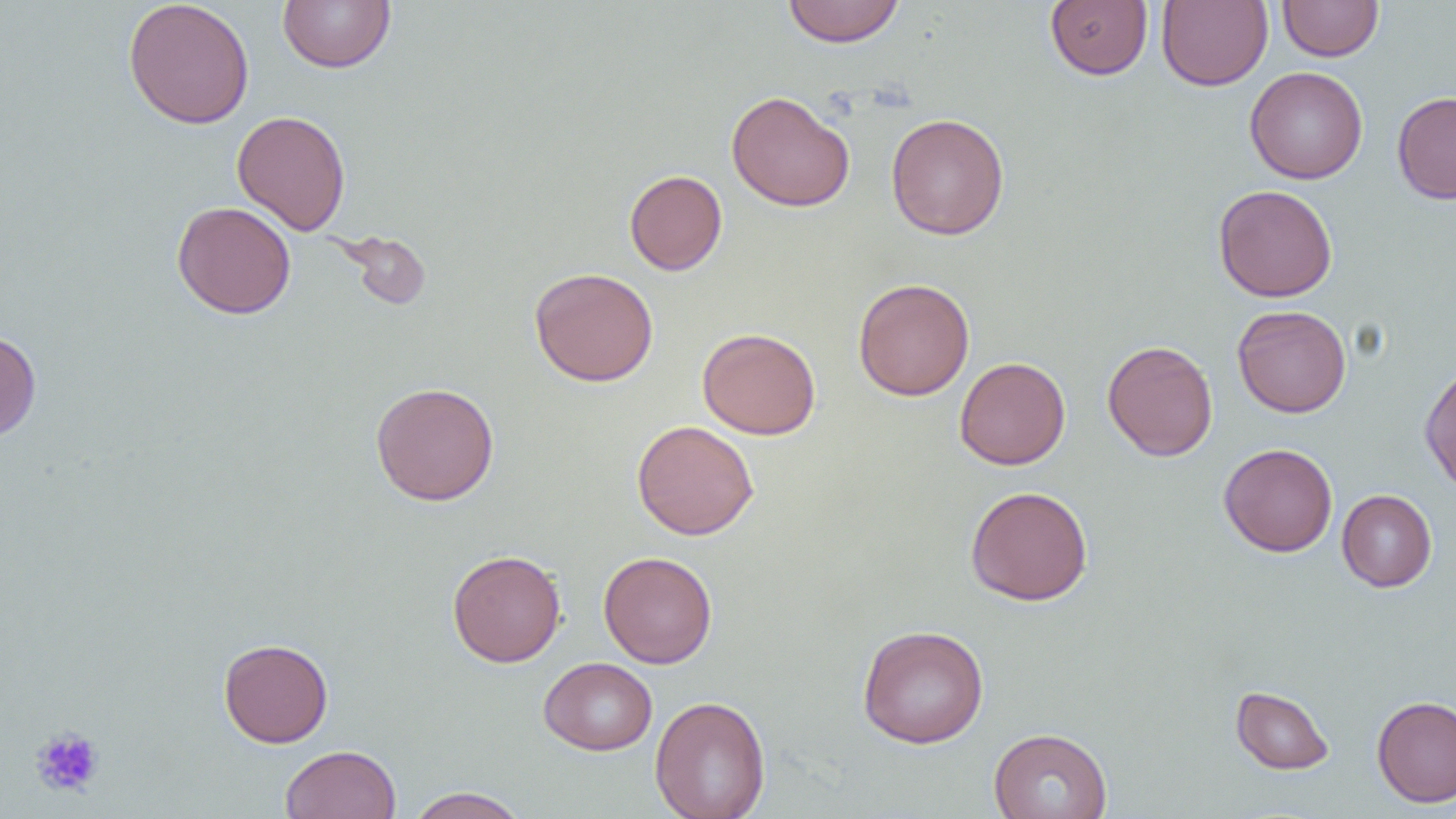
Approximate bounding boxes as named x1/y1/x2/y2 corners in pixels. Platelet locations: (x1=30, y1=726, x2=105, y2=798). Uninfected red blood cell locations: (x1=123, y1=0, x2=255, y2=129), (x1=277, y1=0, x2=396, y2=74), (x1=782, y1=0, x2=906, y2=48), (x1=1045, y1=0, x2=1153, y2=80), (x1=1156, y1=0, x2=1273, y2=91), (x1=1277, y1=1, x2=1383, y2=61), (x1=1244, y1=66, x2=1368, y2=184), (x1=726, y1=90, x2=855, y2=212), (x1=1392, y1=90, x2=1456, y2=204), (x1=231, y1=110, x2=351, y2=235), (x1=885, y1=113, x2=1009, y2=240), (x1=624, y1=170, x2=727, y2=275), (x1=1213, y1=184, x2=1338, y2=303), (x1=171, y1=201, x2=296, y2=319), (x1=332, y1=230, x2=432, y2=311), (x1=529, y1=267, x2=659, y2=387), (x1=853, y1=278, x2=974, y2=401), (x1=1232, y1=304, x2=1351, y2=418), (x1=696, y1=327, x2=821, y2=440), (x1=0, y1=330, x2=42, y2=442), (x1=1102, y1=339, x2=1218, y2=461), (x1=954, y1=356, x2=1070, y2=470), (x1=1419, y1=361, x2=1456, y2=494), (x1=370, y1=381, x2=499, y2=506), (x1=631, y1=420, x2=759, y2=540), (x1=1218, y1=443, x2=1338, y2=557), (x1=964, y1=485, x2=1094, y2=606), (x1=1336, y1=489, x2=1437, y2=592), (x1=447, y1=549, x2=567, y2=668), (x1=598, y1=551, x2=718, y2=668), (x1=857, y1=624, x2=989, y2=748), (x1=218, y1=638, x2=333, y2=747), (x1=539, y1=657, x2=657, y2=755), (x1=1230, y1=685, x2=1335, y2=775), (x1=650, y1=695, x2=771, y2=819), (x1=1372, y1=695, x2=1456, y2=808), (x1=988, y1=727, x2=1112, y2=819), (x1=280, y1=744, x2=401, y2=819), (x1=404, y1=786, x2=531, y2=819). Slide-level diagnosis: negative for blood parasites. Thin blood film. 1000x magnification. Optical microscopy. Image is 1456×819 pixels. Single field of view.